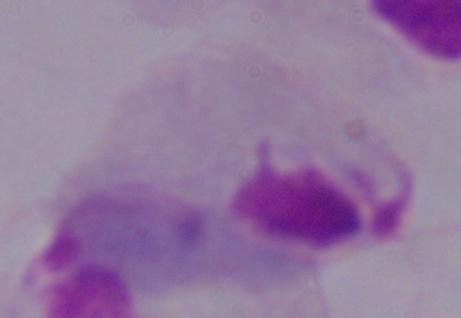
1000x magnification. Micrograph. A trichomonad is shown.